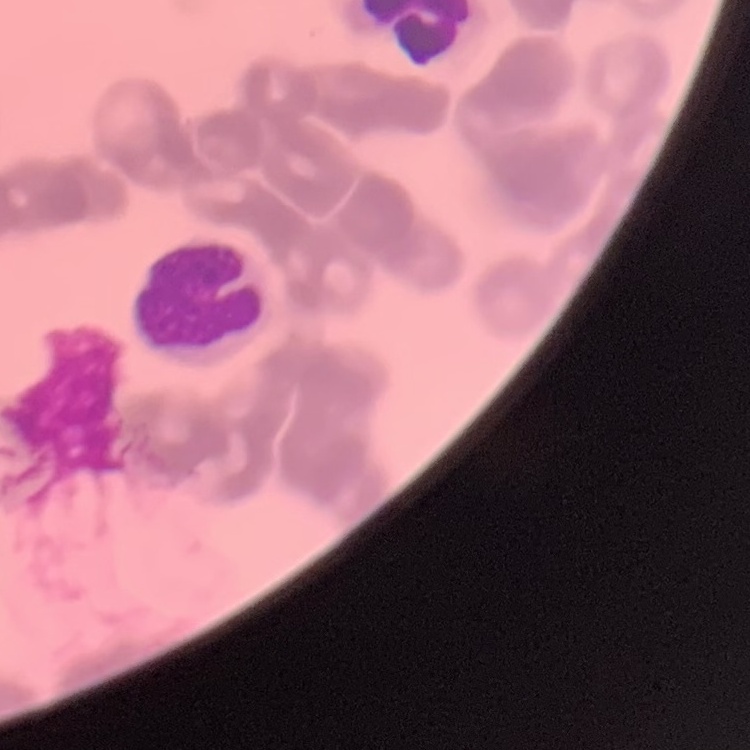
erythrocyte morphology = rouleaux formation
image type = square crop of a larger photomicrograph
preparation = thin blood film
stain = Field's or Giemsa